Name the cell type shown.
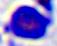

This is a leukocyte.

modality = micrograph
magnification = 400x